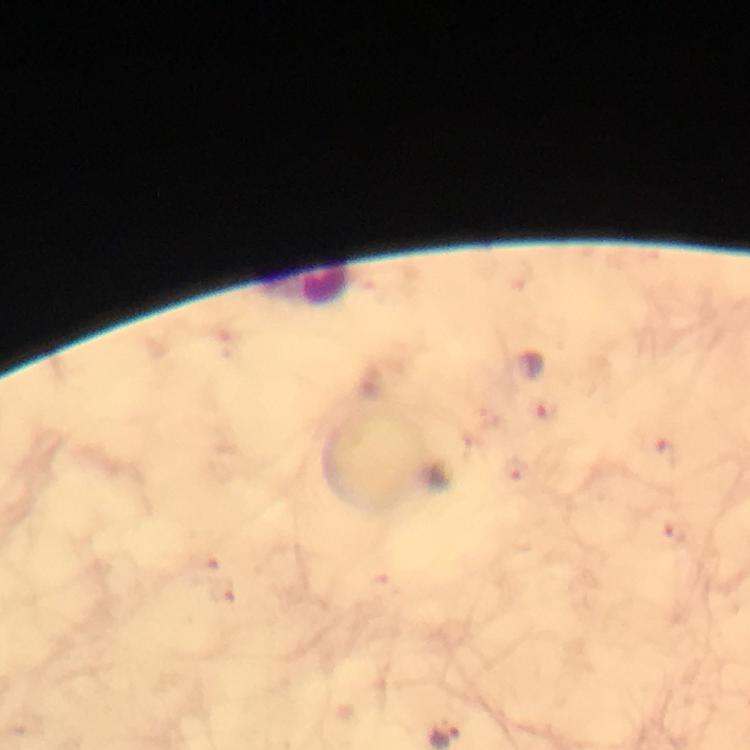
capture = smartphone mounted on the microscope
image size = 750×750 pixels
magnification = 100x
cropped from = a single field of view
immersion oil = applied
preparation = thick smear
Plasmodium parasite locations = approximate centers as {x, y} in pixels: {548, 410}, {668, 453}, {515, 471}, {673, 532}, {226, 593}
context = from a diagnostic examination for malaria
stain = Giemsa